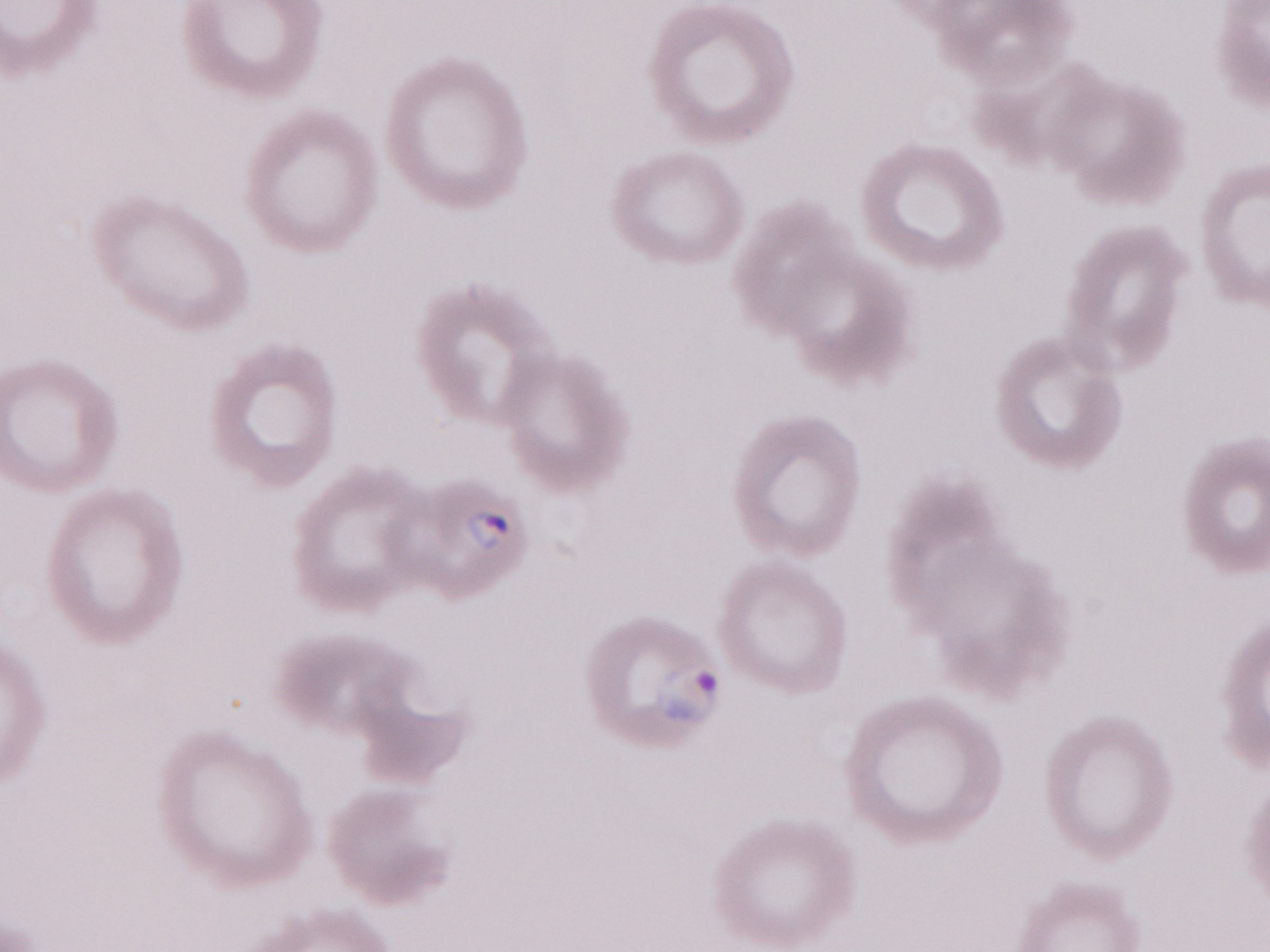 Olympus BX43 microscope and DP73 digital camera. Patient-level malaria diagnosis: positive. Magnification: 1,000x. Image is 1270×952 pixels. One field of this slide. Thin blood film. May-Grünwald-Giemsa stain.